Point out each malaria parasite and each leukocyte.
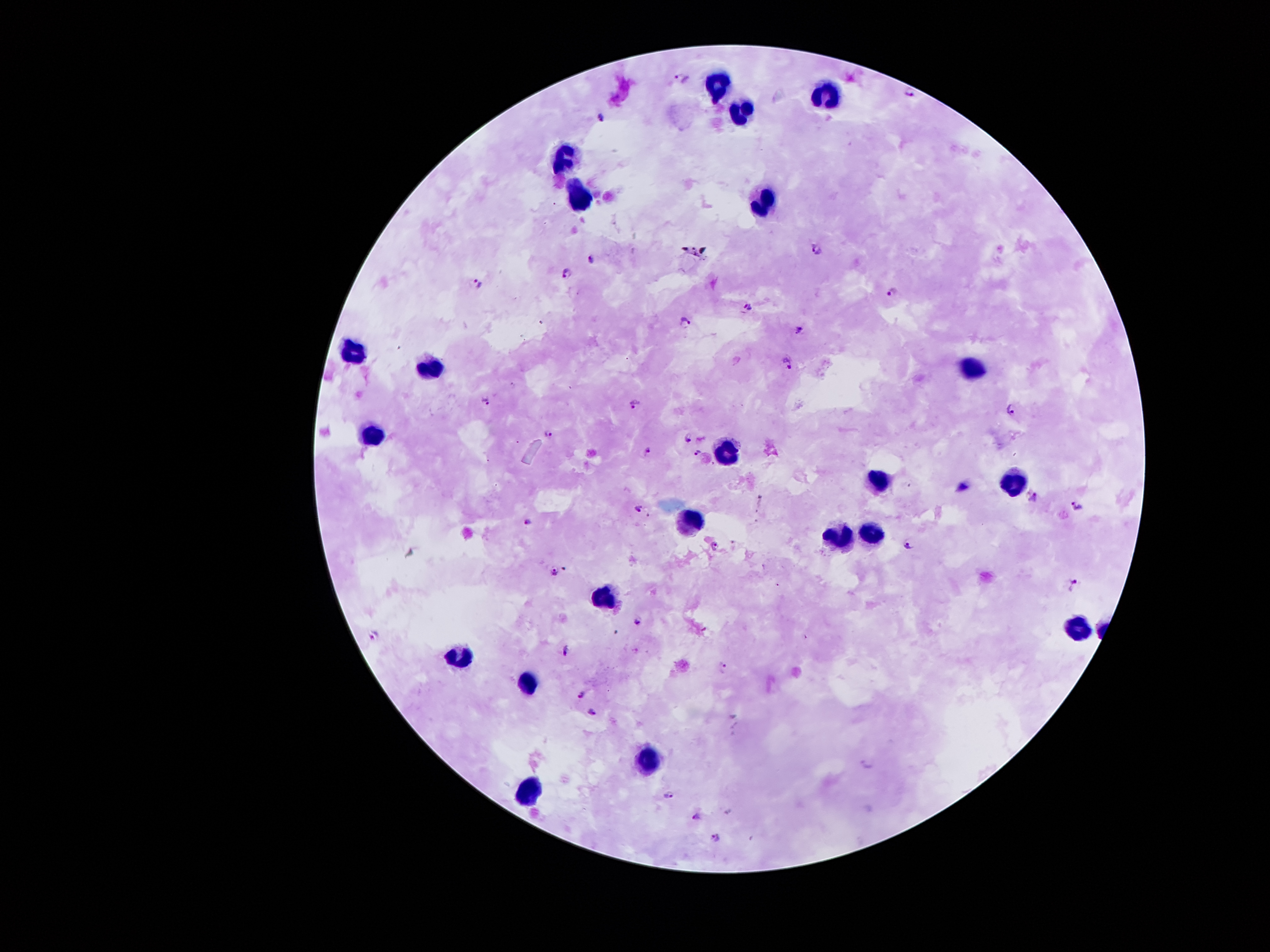

Approximate centers as (x, y) in pixels.
Malaria parasites: (683, 77), (911, 91), (605, 117), (818, 249), (594, 259), (567, 273), (478, 284), (891, 292), (747, 305), (685, 322), (799, 330), (789, 364), (486, 400), (635, 406), (1009, 409), (549, 434), (687, 436), (697, 452), (646, 453), (1033, 497), (1078, 507), (638, 510), (526, 522), (714, 546), (907, 547), (555, 572), (1075, 586), (639, 620), (375, 636), (565, 650), (723, 668), (580, 693), (593, 711), (866, 764), (669, 794), (698, 815), (714, 837).
Leukocytes: (717, 82), (825, 92), (740, 114), (564, 153), (579, 191), (766, 206), (353, 352), (433, 364), (975, 368), (370, 434), (727, 451), (878, 477), (1017, 482), (690, 524), (873, 532), (839, 538), (606, 596), (1078, 628), (459, 656), (532, 681), (647, 760), (525, 788).

Smartphone photograph taken through the microscope eyepiece. Thick blood film. Giemsa stain. 100x magnification. Single field of view. Image is 1270×952 pixels. Patient malaria status: infected with Plasmodium falciparum.